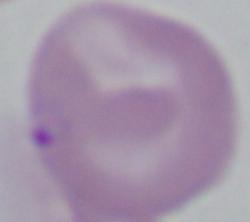
magnification = 1000x
modality = micrograph
identification = Babesia